Locate and identify every blood parasite.
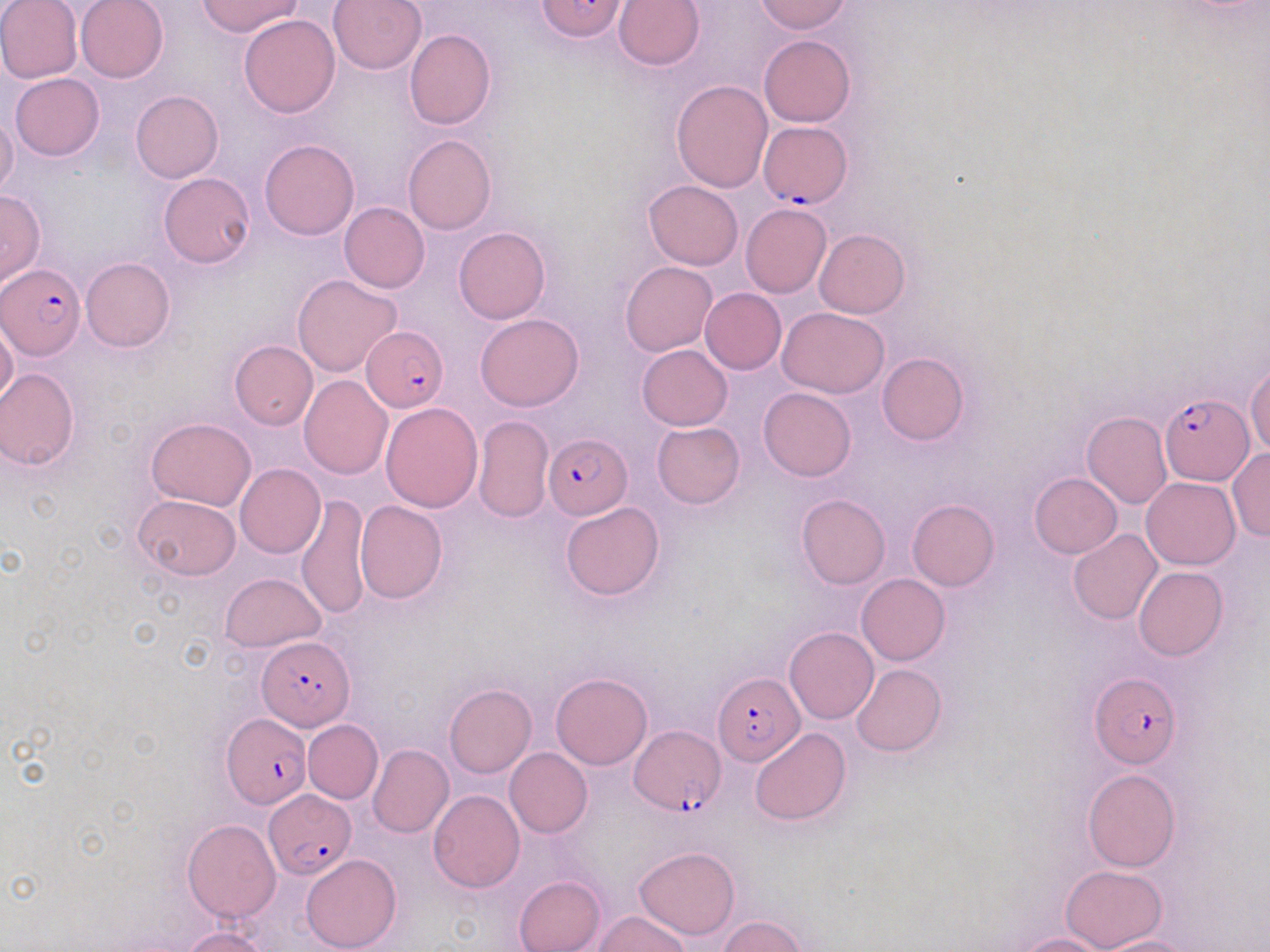

Approximate bounding boxes as (x1, y1, x2, y2) in pixels.
Plasmodium falciparum-infected red blood cells: (759, 120, 852, 208), (1, 263, 86, 359), (361, 325, 449, 412), (1160, 394, 1251, 484), (543, 431, 632, 519), (259, 637, 352, 730), (714, 672, 804, 764), (1090, 672, 1180, 766), (221, 713, 312, 808), (631, 726, 724, 815), (263, 789, 357, 877).
No Plasmodium ovale, Plasmodium malariae, Plasmodium vivax, Babesia divergens, or Trypanosoma brucei observed.

slide-level diagnosis = Plasmodium falciparum
image size = 1270×952 pixels
uninfected red blood cell locations = approximate bounding boxes as (x1, y1, x2, y2) in pixels: (0, 0, 82, 84), (75, 0, 168, 82), (196, 0, 302, 37), (327, 0, 426, 74), (537, 0, 629, 42), (754, 0, 852, 34), (612, 1, 705, 71), (239, 15, 340, 118), (404, 28, 495, 130), (758, 35, 855, 127), (10, 73, 105, 161), (671, 80, 772, 192), (131, 91, 223, 183), (0, 114, 19, 200), (403, 135, 496, 234), (259, 138, 359, 240), (158, 172, 256, 268), (644, 181, 744, 270), (0, 189, 44, 290), (339, 202, 429, 293), (739, 203, 831, 298), (454, 227, 550, 323), (814, 229, 909, 319), (81, 257, 175, 353), (620, 261, 717, 357), (292, 274, 403, 378), (700, 288, 787, 374), (779, 308, 890, 398), (475, 313, 583, 410), (0, 317, 18, 411), (230, 341, 317, 429), (637, 345, 732, 430), (877, 352, 968, 446), (1247, 361, 1270, 455), (0, 368, 80, 470), (299, 374, 392, 478), (759, 387, 856, 482), (381, 402, 483, 512), (1082, 411, 1172, 509), (474, 416, 552, 522), (147, 418, 256, 510), (652, 422, 745, 508), (1228, 449, 1270, 542), (235, 464, 326, 559), (1029, 472, 1122, 558), (1142, 476, 1240, 569), (296, 494, 371, 620), (796, 494, 890, 588), (132, 495, 240, 579), (907, 499, 999, 591), (354, 501, 447, 603), (560, 501, 665, 600), (1068, 529, 1162, 624), (1134, 566, 1227, 661), (219, 573, 326, 653), (857, 574, 950, 665), (784, 627, 878, 724), (850, 664, 947, 756), (551, 674, 652, 769), (444, 683, 536, 777), (303, 719, 383, 803), (750, 727, 851, 825), (368, 744, 453, 837), (504, 748, 592, 837), (1082, 769, 1181, 871), (428, 790, 525, 893), (182, 818, 281, 922), (634, 845, 739, 939), (302, 853, 401, 951), (1060, 864, 1168, 951), (515, 876, 604, 952), (594, 912, 692, 952), (719, 915, 806, 952), (182, 927, 271, 952), (1015, 933, 1111, 952), (1095, 936, 1198, 952)
preparation = thin blood film
modality = light microscopy
magnification = 1000x
stain = May-Grünwald-Giemsa
field of view = one of a larger specimen